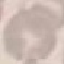

Result: no malaria parasites detected. Thin blood film. Photographed with a smartphone camera at the microscope eyepiece. Giemsa stain. Automatically extracted cell patch, resized to 64 × 64 pixels.